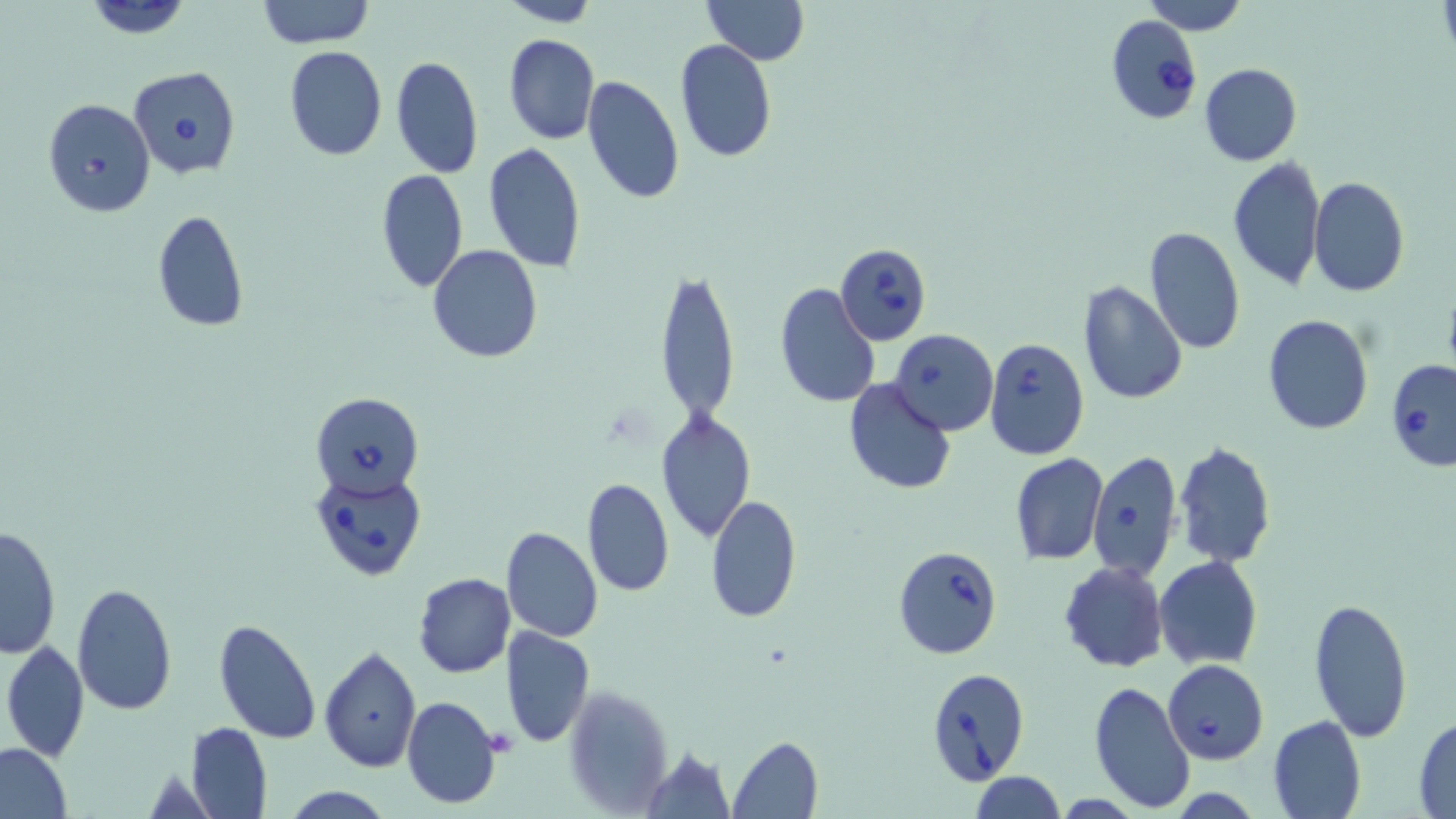

{
  "slide_level_diagnosis": "Babesia divergens",
  "magnification": "1000x",
  "stain": "May-Grünwald-Giemsa",
  "field_of_view": "one of a larger specimen",
  "modality": "optical microscopy",
  "uninfected_red_blood_cell_locations": "approximate bounding boxes as (x1,y1)-(x2,y2) corner pairs in pixels: (83,0)-(194,38), (257,0)-(373,48), (702,0)-(809,65), (1141,0)-(1248,34), (496,1)-(600,27), (503,33)-(600,145), (674,39)-(778,163), (283,47)-(386,161), (390,54)-(484,180), (1199,63)-(1303,166), (581,75)-(686,204), (482,142)-(587,272), (1227,155)-(1326,292), (376,168)-(469,293), (1308,175)-(1410,296), (152,211)-(250,331), (1143,226)-(1246,356), (427,245)-(544,365), (656,268)-(740,427), (1077,278)-(1186,403), (775,282)-(880,407), (1262,315)-(1373,436), (841,377)-(958,494), (656,408)-(756,542), (1173,440)-(1276,569), (1010,453)-(1109,565), (582,477)-(673,597), (705,495)-(801,624), (0,524)-(61,659), (502,527)-(603,642), (1154,556)-(1261,670), (1059,561)-(1168,672), (413,572)-(515,677), (70,583)-(178,716), (1308,596)-(1414,740), (212,618)-(321,742), (500,626)-(595,748), (2,640)-(89,763), (319,646)-(421,771), (1088,681)-(1194,810), (564,683)-(672,814), (402,695)-(502,810), (1267,714)-(1368,818), (1413,715)-(1455,816), (185,722)-(273,818), (729,736)-(824,817), (0,742)-(74,818), (642,745)-(735,817), (970,772)-(1065,817), (277,787)-(397,818)",
  "image_size": "1456×819 pixels",
  "babesia_divergens_infected_red_blood_cell_locations": "approximate bounding boxes as (x1,y1)-(x2,y2) corner pairs in pixels: (1104,12)-(1203,124), (128,67)-(241,180), (43,98)-(155,217), (837,243)-(932,343), (889,328)-(997,436), (984,338)-(1091,461), (1386,361)-(1456,472), (311,392)-(423,497), (1088,450)-(1182,581), (310,470)-(427,581), (892,545)-(1003,659), (1163,659)-(1269,765), (924,667)-(1032,786)",
  "preparation": "thin blood smear",
  "platelet_locations": "approximate bounding boxes as (x1,y1)-(x2,y2) corner pairs in pixels: (482,729)-(518,755)"
}